Name the parasite shown.
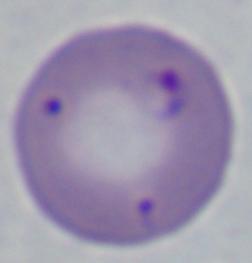
This is Babesia.

Captured at 1000x magnification. Photomicrograph.